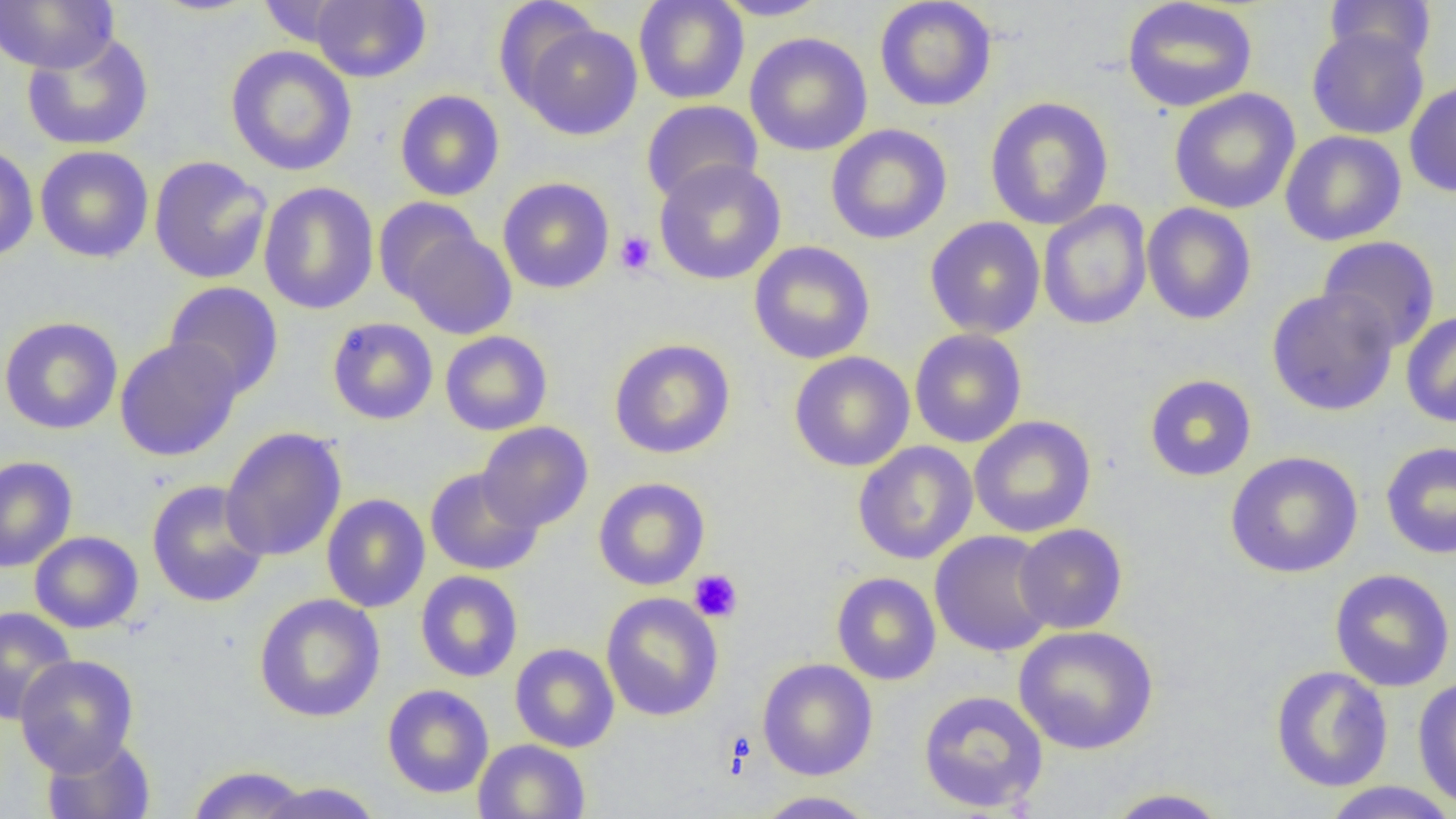

Approximate bounding boxes as [x1, y1, x2, y2] in pixels. Platelet locations: [615, 231, 657, 276], [689, 569, 743, 623], [721, 729, 756, 779]. Uninfected red blood cell locations: [0, 0, 118, 73], [308, 0, 431, 83], [633, 0, 749, 105], [712, 0, 831, 20], [874, 0, 997, 112], [1121, 0, 1258, 112], [1324, 0, 1436, 68], [493, 1, 601, 106], [255, 2, 358, 47], [515, 19, 645, 140], [1307, 27, 1429, 140], [20, 32, 155, 151], [744, 32, 873, 157], [225, 45, 358, 176], [1404, 79, 1456, 198], [1169, 88, 1300, 214], [394, 89, 505, 201], [984, 96, 1114, 230], [640, 100, 762, 205], [825, 124, 953, 245], [1280, 131, 1407, 246], [0, 143, 39, 263], [35, 145, 154, 263], [148, 156, 272, 284], [653, 159, 786, 285], [497, 177, 615, 294], [258, 181, 379, 315], [373, 197, 484, 305], [1038, 200, 1152, 331], [1141, 203, 1257, 325], [925, 216, 1046, 339], [400, 226, 517, 339], [1317, 236, 1441, 352], [748, 241, 876, 364], [163, 281, 284, 400], [1266, 287, 1399, 416], [1400, 310, 1456, 428], [0, 316, 123, 435], [326, 317, 438, 425], [909, 328, 1027, 448], [440, 330, 553, 436], [114, 337, 243, 461], [609, 338, 736, 460], [789, 351, 915, 472], [1144, 374, 1257, 482], [969, 416, 1097, 538], [478, 422, 593, 532], [220, 427, 347, 562], [852, 441, 978, 564], [1381, 441, 1456, 559], [1225, 451, 1364, 578], [0, 456, 78, 572], [424, 467, 543, 576], [593, 477, 710, 590], [146, 480, 269, 608], [321, 494, 430, 613], [1014, 523, 1128, 634], [29, 530, 144, 633], [929, 530, 1058, 657], [1329, 568, 1455, 692], [415, 570, 523, 682], [831, 572, 941, 685], [600, 592, 724, 722], [253, 593, 386, 722], [0, 606, 78, 725], [1013, 625, 1158, 755], [510, 643, 620, 753], [14, 654, 139, 775], [758, 658, 878, 781], [1270, 665, 1393, 793], [1412, 675, 1456, 810], [381, 684, 494, 799], [917, 689, 1049, 814], [40, 734, 157, 819], [473, 739, 590, 819], [185, 765, 312, 819], [255, 781, 384, 819], [1319, 782, 1455, 819], [1103, 787, 1232, 817], [753, 791, 880, 818]. Slide-level diagnosis: negative for blood parasites. Single field of view. Image is 1456×819 pixels. Thin blood smear. Captured at 1000x magnification. Optical microscopy.